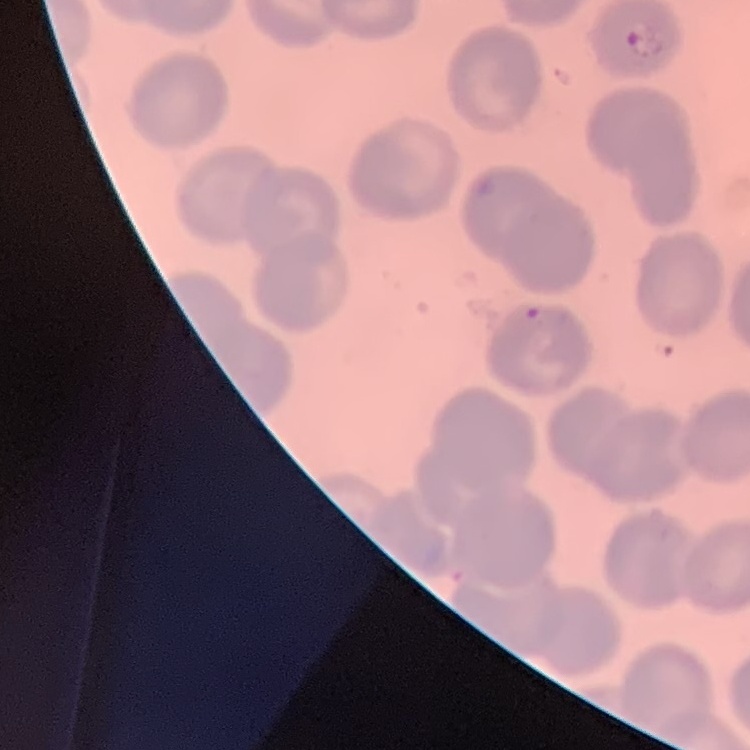 The erythrocytes show no rouleaux formation. Stained with either Field's or Giemsa. Thin peripheral smear. Square crop of a larger photomicrograph.